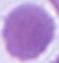

Summary:
  - Identification: red blood cell
  - Modality: photomicrograph
  - Magnification: 1000x